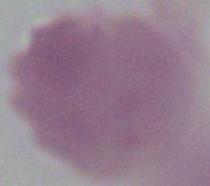

Summary:
  - Identification: erythrocyte
  - Modality: micrograph
  - Magnification: 1000x